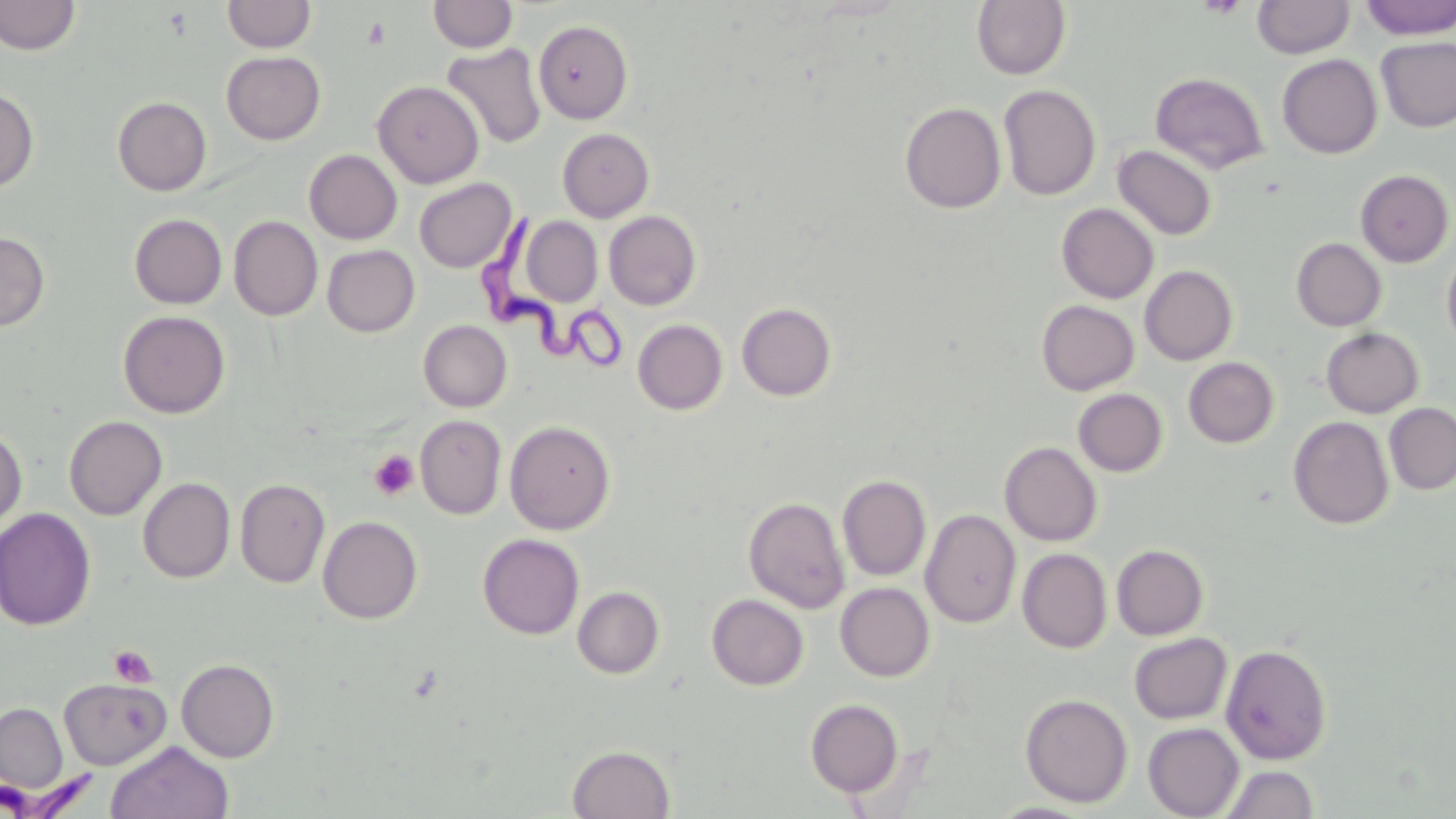

slide-level diagnosis = Trypanosoma brucei
image size = 1456×819 pixels
platelet locations = approximate bounding boxes as (x1, y1, x2, y2) in pixels: (363, 17, 390, 49), (369, 449, 419, 500), (108, 645, 157, 688)
preparation = thin blood smear
uninfected red blood cell locations = approximate bounding boxes as (x1, y1, x2, y2) in pixels: (0, 0, 81, 56), (428, 0, 519, 53), (1359, 0, 1456, 40), (222, 1, 316, 53), (971, 1, 1071, 80), (1252, 1, 1354, 59), (533, 20, 633, 123), (1376, 36, 1456, 132), (442, 43, 547, 149), (221, 51, 326, 145), (1277, 54, 1382, 158), (1150, 71, 1269, 174), (372, 81, 485, 188), (998, 84, 1101, 201), (0, 86, 38, 192), (112, 97, 212, 195), (899, 102, 1006, 213), (557, 128, 654, 222), (1112, 145, 1217, 241), (304, 150, 402, 244), (1356, 170, 1454, 267), (414, 178, 517, 272), (1056, 203, 1158, 303), (604, 211, 701, 310), (129, 213, 227, 309), (229, 216, 322, 321), (521, 217, 603, 306), (0, 232, 50, 332), (1291, 238, 1387, 331), (1441, 244, 1456, 354), (322, 245, 420, 337), (1140, 265, 1238, 365), (1036, 300, 1139, 395), (736, 303, 837, 401), (118, 310, 231, 418), (633, 319, 727, 415), (418, 320, 512, 411), (1320, 327, 1424, 418), (1183, 357, 1279, 447), (1073, 388, 1168, 477), (1384, 403, 1456, 495), (64, 415, 167, 520), (415, 415, 507, 519), (1288, 416, 1394, 529), (505, 420, 615, 535), (0, 425, 27, 535), (999, 442, 1102, 546), (837, 474, 932, 581), (138, 478, 235, 583), (235, 478, 330, 588), (744, 496, 850, 614), (0, 507, 96, 631), (921, 509, 1021, 628), (318, 516, 422, 624), (478, 534, 584, 639), (1111, 544, 1208, 640), (1017, 549, 1112, 653), (835, 582, 934, 681), (572, 586, 665, 679), (706, 594, 809, 690), (1129, 633, 1232, 724), (1221, 644, 1333, 764), (176, 659, 279, 763), (59, 678, 171, 770), (1019, 693, 1133, 808), (805, 699, 904, 797), (1, 702, 68, 793), (1143, 723, 1244, 818), (106, 740, 234, 819), (567, 745, 675, 819), (1221, 764, 1319, 819)
magnification = 1000x
modality = light microscopy
stain = May-Grünwald-Giemsa
field of view = single
Trypanosoma brucei locations = approximate bounding boxes as (x1, y1, x2, y2) in pixels: (483, 219, 630, 369), (1, 762, 99, 818)